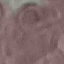
Summary:
  - Result: no malaria parasites seen
  - Image type: cell patch, automatically extracted from a larger field of view and resized to 64 × 64 pixels
  - Preparation: thin smear
  - Stain: Giemsa
  - Capture: smartphone through the microscope eyepiece